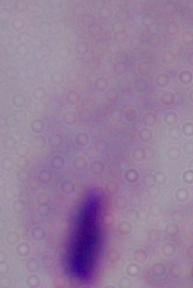
Summary:
  - Identification: trichomonad
  - Magnification: 1000x
  - Modality: micrograph